Report the malaria status of this cell.
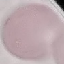
Uninfected.

{
  "capture": "smartphone camera at the microscope eyepiece",
  "preparation": "thin blood smear",
  "image_type": "cell patch, automatically extracted from a larger field of view and resized to 64 × 64 pixels",
  "stain": "Giemsa"
}